Outline each Plasmodium falciparum-infected red blood cell.
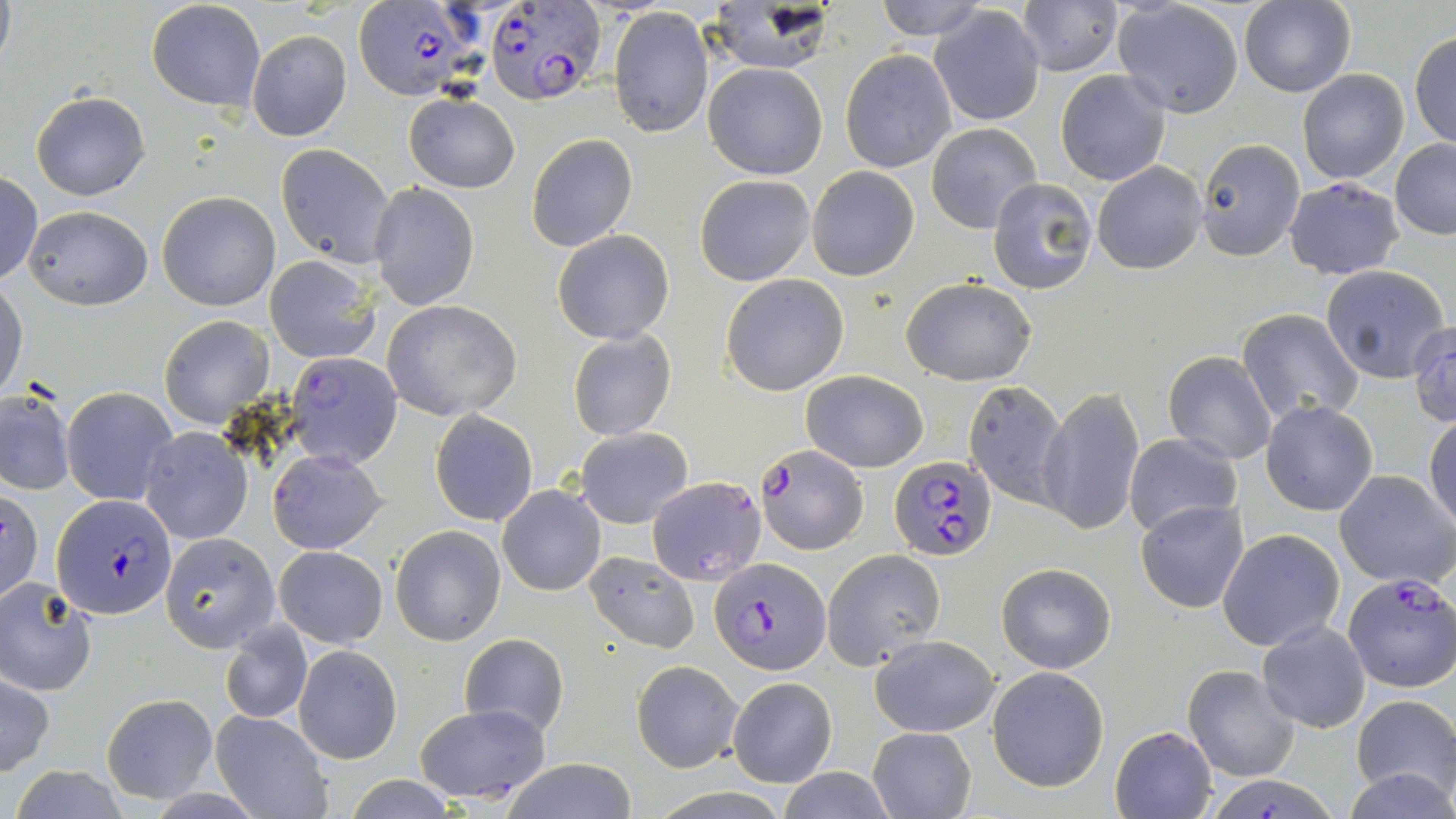

Approximate bounding boxes as (x1, y1, x2, y2) in pixels.
Plasmodium falciparum-infected red blood cells: (483, 1, 607, 105), (354, 2, 483, 102), (755, 443, 868, 555), (891, 453, 997, 560), (53, 493, 176, 616), (713, 557, 830, 673), (1343, 573, 1456, 692).

Summary:
  - Uninfected red blood cell locations: (870, 0, 991, 41), (147, 1, 265, 113), (1016, 1, 1121, 76), (1238, 1, 1356, 97), (710, 2, 834, 72), (1111, 4, 1242, 119), (609, 7, 713, 139), (931, 7, 1046, 126), (247, 29, 352, 141), (1410, 32, 1456, 150), (840, 49, 958, 174), (704, 62, 828, 181), (1297, 67, 1410, 185), (1056, 70, 1170, 185), (31, 91, 152, 201), (404, 92, 519, 193), (926, 123, 1042, 233), (526, 133, 639, 253), (1196, 139, 1305, 260), (1390, 141, 1456, 238), (277, 146, 397, 268), (1092, 161, 1209, 275), (807, 167, 918, 281), (0, 172, 43, 287), (695, 174, 815, 285), (986, 178, 1096, 295), (1284, 178, 1404, 277), (370, 182, 480, 312), (157, 191, 280, 312), (22, 205, 154, 310), (552, 228, 675, 345), (264, 255, 380, 365), (1319, 265, 1452, 385), (720, 274, 849, 395), (902, 277, 1037, 385), (0, 281, 27, 405), (383, 300, 523, 422), (1238, 309, 1365, 426), (157, 316, 274, 428), (1407, 322, 1456, 428), (567, 329, 677, 441), (285, 351, 402, 469), (1162, 351, 1278, 465), (800, 369, 928, 472), (963, 381, 1067, 505), (1, 385, 76, 498), (62, 386, 177, 504), (1037, 386, 1146, 537), (1260, 400, 1378, 516), (431, 409, 538, 526), (1425, 414, 1456, 532), (574, 427, 694, 528), (141, 428, 252, 544), (1124, 433, 1242, 537), (268, 449, 387, 555), (1333, 470, 1455, 588), (648, 476, 766, 587), (498, 485, 605, 596), (1, 487, 44, 604), (1136, 501, 1251, 613), (391, 526, 505, 645), (1218, 528, 1345, 651), (161, 532, 278, 653), (275, 545, 388, 648), (822, 549, 945, 668), (584, 551, 699, 651), (996, 562, 1117, 674), (0, 582, 98, 695), (221, 620, 312, 724), (1256, 620, 1370, 733), (460, 633, 568, 739), (869, 636, 998, 737), (294, 644, 402, 764), (631, 659, 742, 772), (1184, 665, 1299, 781), (987, 666, 1109, 791), (0, 672, 53, 775), (728, 676, 838, 787), (103, 693, 216, 803), (1351, 694, 1455, 801), (412, 702, 554, 802), (211, 710, 331, 819), (1110, 724, 1218, 818), (869, 727, 976, 818), (497, 759, 641, 818), (1346, 765, 1454, 819), (338, 776, 464, 818)
  - Slide-level diagnosis: Plasmodium falciparum
  - Field of view: one of a larger specimen
  - Image size: 1456×819 pixels
  - Preparation: thin blood film
  - Stain: May-Grünwald-Giemsa
  - Modality: light microscopy
  - Magnification: 1000x